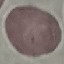 Result: negative for malaria parasites. Cell patch, automatically extracted from a larger field of view and resized to 64 × 64 pixels. Photographed with a smartphone camera at the microscope eyepiece. Giemsa stain. Thin blood smear.